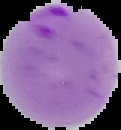

image size = 121×130 pixels
result = Plasmodium parasites detected
preparation = thin blood smear
image type = cell region segmented out of the field of view; surrounding area masked to black